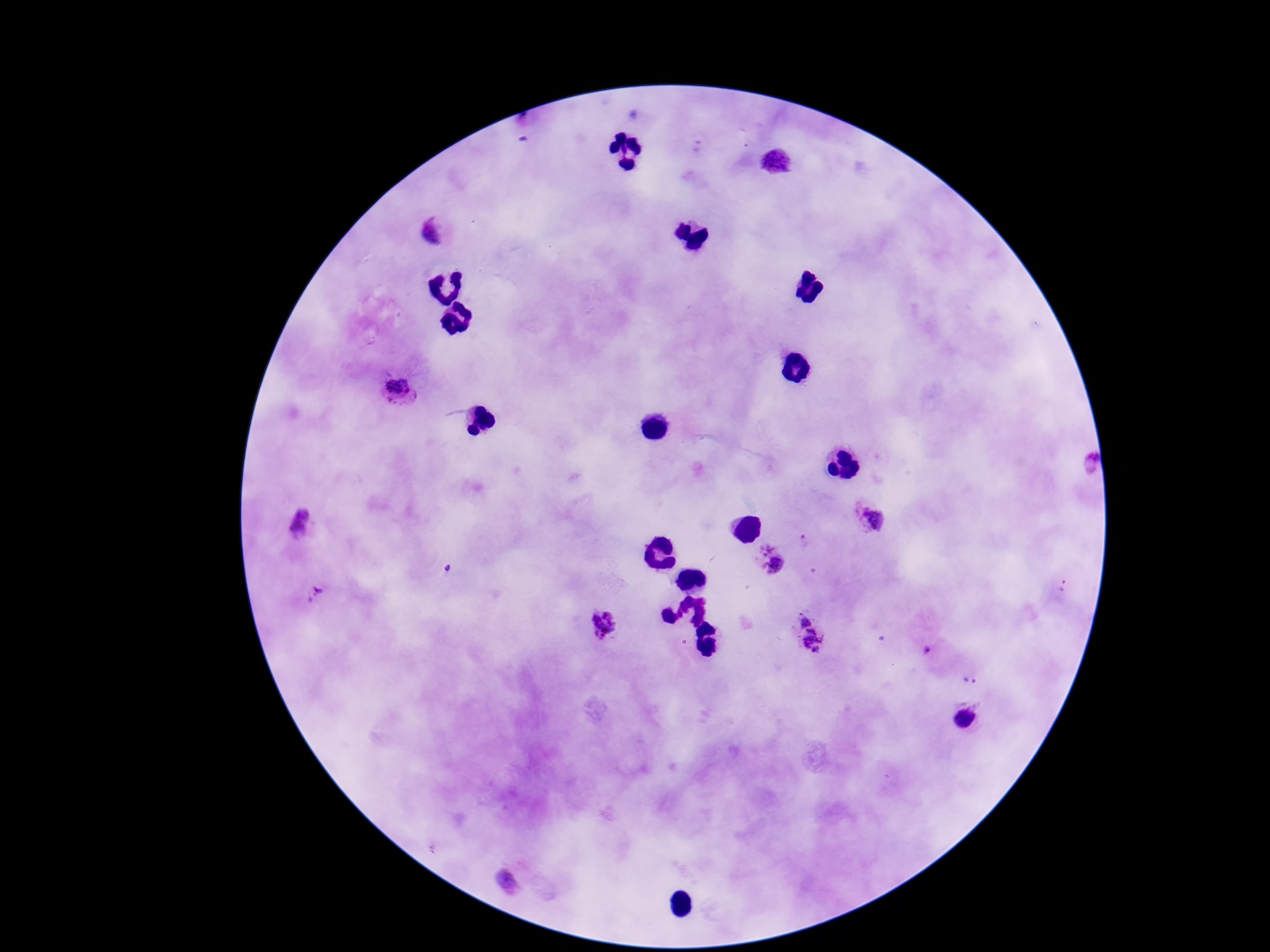

Approximate centers as {x, y} in pixels. Plasmodium parasite locations: {776, 162}, {433, 231}, {400, 391}, {1087, 465}, {870, 519}, {301, 527}, {806, 542}, {770, 558}, {1065, 587}, {312, 593}, {603, 623}, {810, 634}, {925, 651}, {970, 681}, {964, 719}, {507, 879}. Image is 1270×952 pixels. Giemsa stain. Photographed through the microscope eyepiece with a smartphone camera. 100x magnification. Patient malaria status: infected. Thick peripheral-blood smear. Single field of view.